Identify the preparation type.
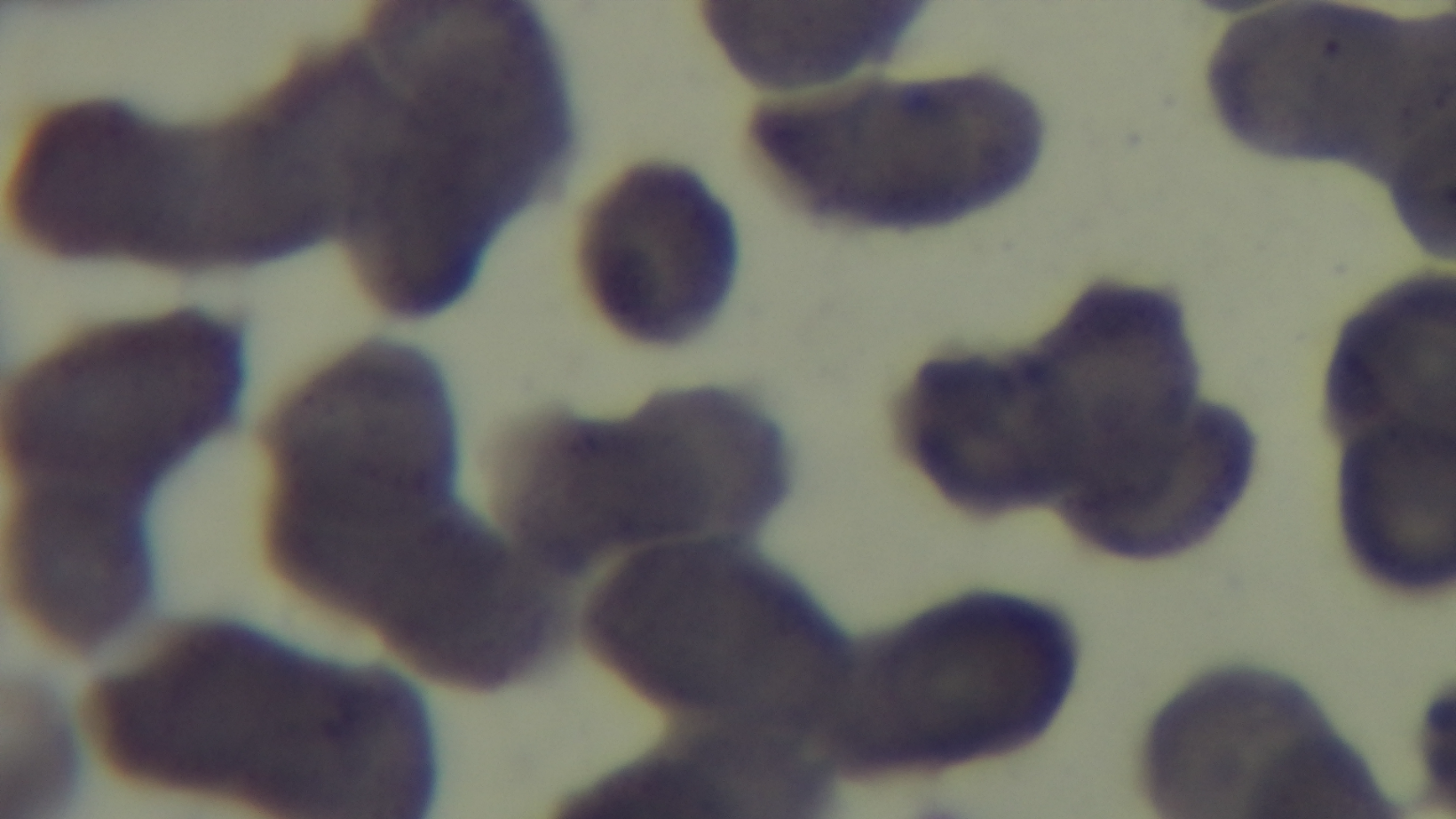
A thin smear.

Summary:
  - Stain: Giemsa
  - Malaria status: negative
  - Objective: 100x oil immersion
  - Modality: light microscopy
  - Field of view: single
  - Capture: mounted 4K digital camera